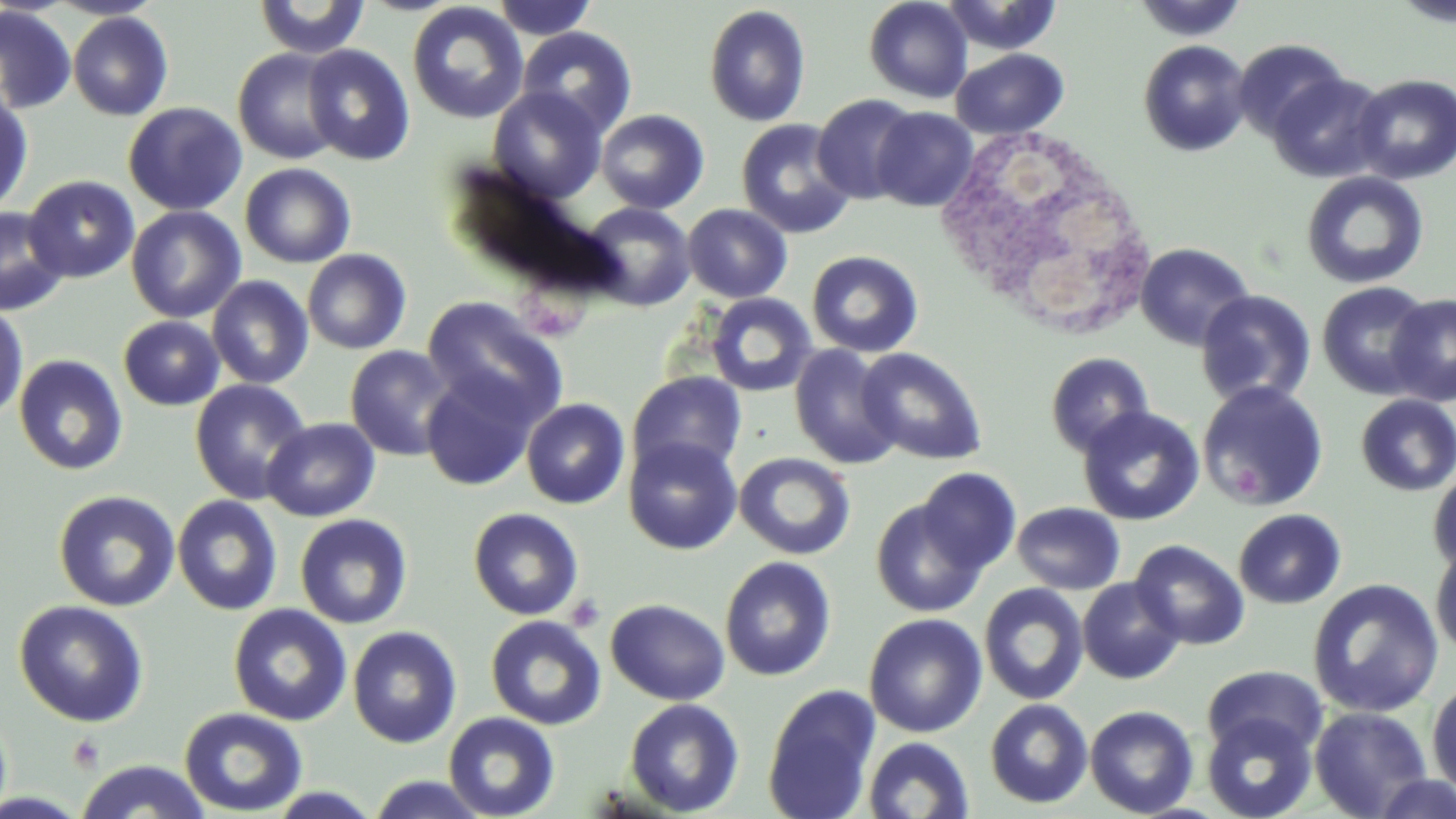

Approximate bounding boxes as named x1/y1/x2/y2 corners in pixels. Platelet locations: (x1=1232, y1=462, x2=1264, y2=505), (x1=565, y1=593, x2=606, y2=632), (x1=68, y1=734, x2=105, y2=772). Uninfected red blood cell locations: (x1=253, y1=0, x2=371, y2=59), (x1=490, y1=0, x2=598, y2=40), (x1=863, y1=0, x2=973, y2=104), (x1=939, y1=0, x2=1063, y2=55), (x1=1392, y1=0, x2=1456, y2=27), (x1=1136, y1=1, x2=1250, y2=44), (x1=406, y1=2, x2=530, y2=124), (x1=703, y1=5, x2=812, y2=127), (x1=0, y1=6, x2=77, y2=115), (x1=68, y1=12, x2=173, y2=121), (x1=516, y1=26, x2=638, y2=138), (x1=1232, y1=38, x2=1350, y2=141), (x1=1138, y1=39, x2=1252, y2=156), (x1=302, y1=44, x2=415, y2=166), (x1=233, y1=47, x2=345, y2=165), (x1=951, y1=48, x2=1069, y2=139), (x1=1267, y1=72, x2=1389, y2=183), (x1=1351, y1=74, x2=1456, y2=184), (x1=0, y1=87, x2=34, y2=218), (x1=487, y1=87, x2=607, y2=204), (x1=813, y1=93, x2=920, y2=205), (x1=122, y1=102, x2=247, y2=216), (x1=871, y1=107, x2=978, y2=212), (x1=595, y1=109, x2=709, y2=214), (x1=736, y1=118, x2=857, y2=239), (x1=239, y1=163, x2=356, y2=268), (x1=1301, y1=171, x2=1429, y2=289), (x1=23, y1=175, x2=140, y2=283), (x1=581, y1=202, x2=696, y2=312), (x1=682, y1=204, x2=792, y2=303), (x1=0, y1=206, x2=69, y2=316), (x1=126, y1=206, x2=246, y2=324), (x1=1135, y1=242, x2=1255, y2=351), (x1=302, y1=249, x2=412, y2=354), (x1=807, y1=250, x2=924, y2=357), (x1=206, y1=275, x2=314, y2=390), (x1=1316, y1=280, x2=1435, y2=400), (x1=1195, y1=290, x2=1316, y2=408), (x1=705, y1=292, x2=818, y2=397), (x1=1385, y1=294, x2=1456, y2=407), (x1=421, y1=296, x2=569, y2=427), (x1=0, y1=301, x2=29, y2=424), (x1=118, y1=315, x2=225, y2=411), (x1=344, y1=344, x2=458, y2=461), (x1=788, y1=344, x2=903, y2=470), (x1=855, y1=347, x2=988, y2=466), (x1=1045, y1=351, x2=1154, y2=458), (x1=13, y1=354, x2=128, y2=476), (x1=419, y1=370, x2=541, y2=492), (x1=627, y1=371, x2=748, y2=481), (x1=189, y1=379, x2=312, y2=504), (x1=1196, y1=380, x2=1329, y2=512), (x1=1355, y1=394, x2=1456, y2=496), (x1=521, y1=398, x2=630, y2=510), (x1=1077, y1=406, x2=1204, y2=526), (x1=262, y1=417, x2=380, y2=522), (x1=623, y1=436, x2=742, y2=555), (x1=734, y1=452, x2=856, y2=560), (x1=915, y1=467, x2=1021, y2=576), (x1=1427, y1=467, x2=1456, y2=577), (x1=52, y1=489, x2=181, y2=612), (x1=171, y1=495, x2=284, y2=616), (x1=871, y1=498, x2=988, y2=618), (x1=1011, y1=502, x2=1125, y2=595), (x1=467, y1=507, x2=584, y2=620), (x1=1233, y1=508, x2=1346, y2=609), (x1=294, y1=513, x2=413, y2=629), (x1=1130, y1=539, x2=1250, y2=650), (x1=1430, y1=542, x2=1456, y2=659), (x1=719, y1=556, x2=837, y2=681), (x1=1077, y1=578, x2=1185, y2=684), (x1=1307, y1=578, x2=1444, y2=718), (x1=979, y1=583, x2=1089, y2=706), (x1=605, y1=598, x2=730, y2=706), (x1=13, y1=599, x2=149, y2=727), (x1=228, y1=604, x2=352, y2=726), (x1=863, y1=613, x2=987, y2=738), (x1=485, y1=615, x2=607, y2=730), (x1=347, y1=626, x2=462, y2=749), (x1=1202, y1=665, x2=1327, y2=760), (x1=1426, y1=676, x2=1456, y2=801), (x1=762, y1=684, x2=882, y2=819), (x1=624, y1=698, x2=745, y2=816), (x1=985, y1=698, x2=1093, y2=808), (x1=1084, y1=705, x2=1199, y2=817), (x1=1309, y1=706, x2=1433, y2=819), (x1=179, y1=707, x2=308, y2=816), (x1=443, y1=711, x2=561, y2=819), (x1=1202, y1=711, x2=1319, y2=819), (x1=863, y1=736, x2=975, y2=819), (x1=74, y1=759, x2=213, y2=819), (x1=1369, y1=773, x2=1456, y2=817), (x1=364, y1=774, x2=493, y2=817), (x1=262, y1=787, x2=385, y2=818). White blood cell locations: (x1=940, y1=129, x2=1149, y2=338). Slide-level diagnosis: no evidence of blood parasites. May-Grünwald-Giemsa-stained preparation. Single field of view. Thin blood smear. Captured at 1000x magnification. Light microscopy. Image is 1456×819 pixels.